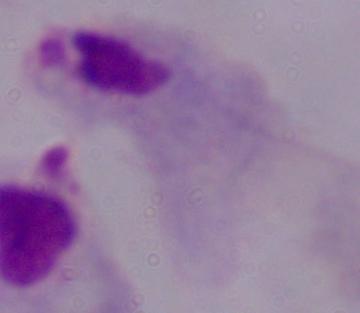 Photomicrograph. A trichomonad is shown. 1000x magnification.